Classify this cell by malaria status.
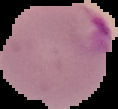
Parasitized.

image_type: segmented cell region with the area outside set to black
image_size: 118×109 pixels
preparation: thin blood smear